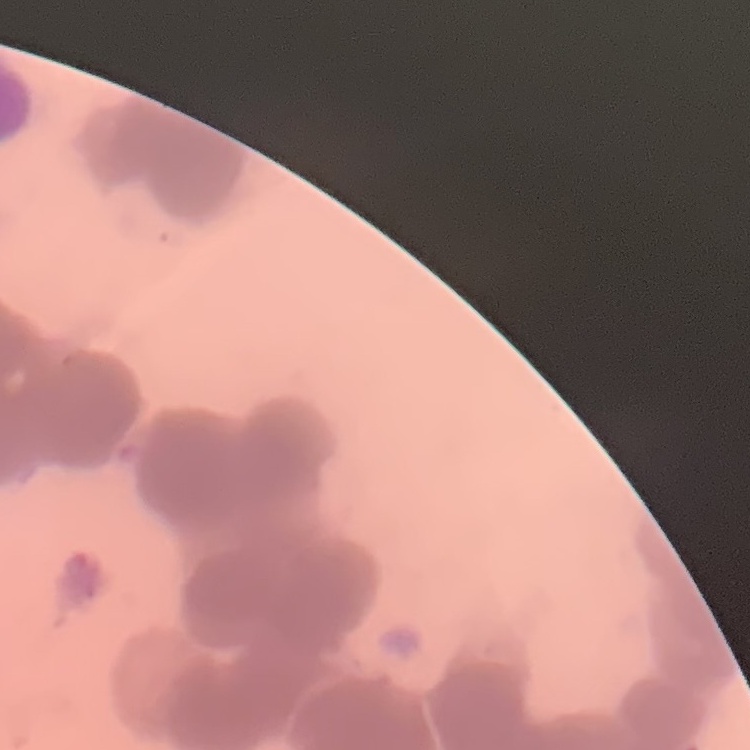
Summary:
  - Erythrocyte morphology: rouleaux formation
  - Image type: square crop of a larger photomicrograph
  - Stain: Field's or Giemsa
  - Preparation: thin blood smear